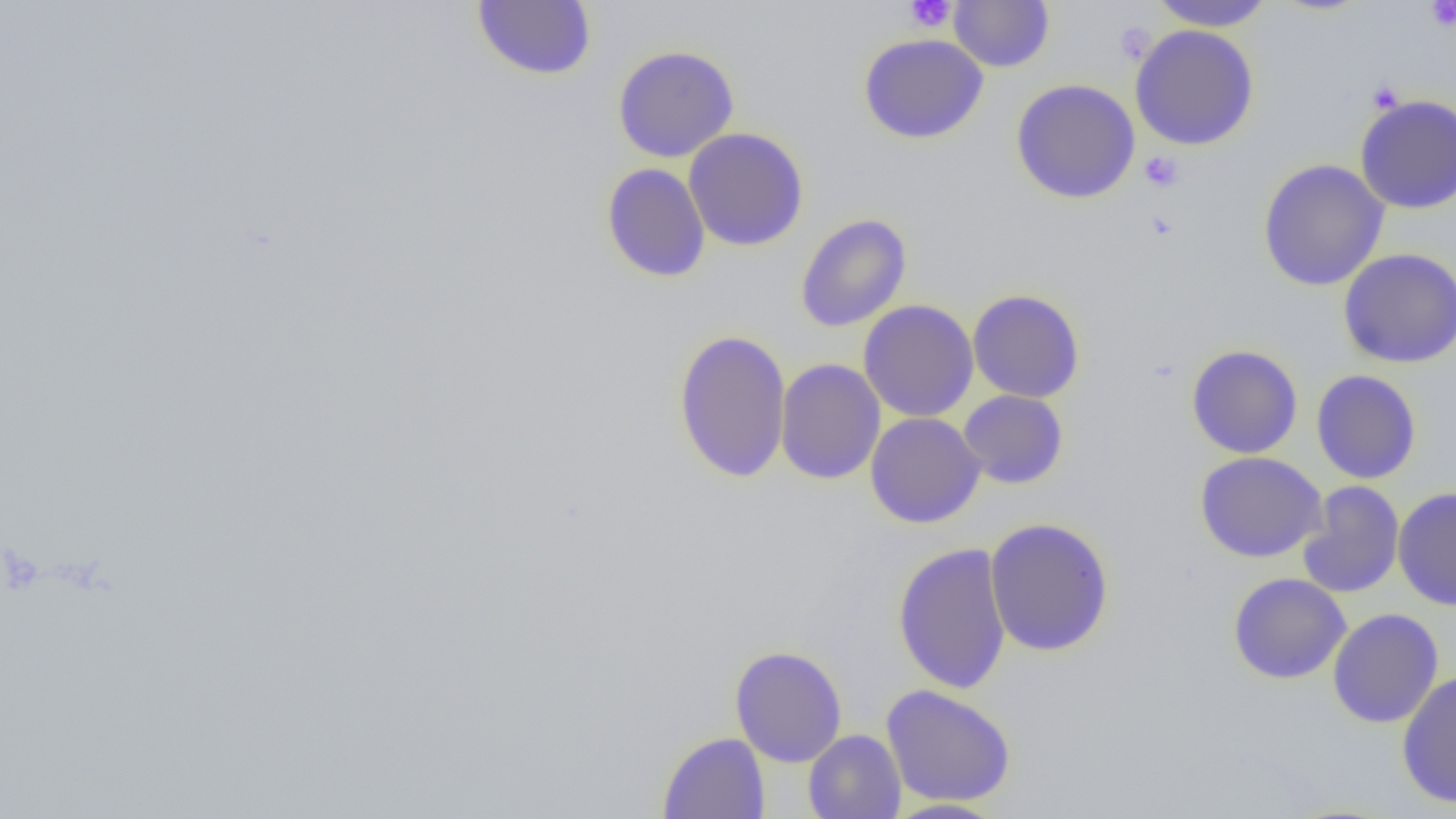
Summary:
  - Coordinate format: approximate bounding boxes as [x1, y1, x2, y2] in pixels
  - Platelet locations: [904, 0, 956, 32], [1425, 0, 1456, 31], [1116, 22, 1156, 65], [1139, 150, 1185, 193]
  - Uninfected red blood cell locations: [471, 0, 597, 82], [949, 0, 1054, 72], [1149, 0, 1274, 31], [1130, 24, 1259, 150], [858, 33, 989, 144], [612, 45, 739, 162], [1011, 78, 1141, 204], [1355, 94, 1456, 213], [683, 128, 809, 252], [1257, 158, 1390, 291], [601, 162, 711, 283], [795, 213, 912, 332], [1338, 248, 1456, 368], [968, 289, 1085, 403], [858, 299, 979, 422], [672, 328, 792, 483], [1186, 344, 1303, 459], [775, 358, 886, 485], [1311, 369, 1422, 484], [958, 390, 1068, 489], [865, 411, 986, 528], [1195, 451, 1326, 562], [1297, 481, 1405, 599], [1393, 487, 1456, 611], [985, 517, 1115, 657], [892, 542, 1012, 694], [1228, 572, 1351, 684], [1327, 608, 1444, 728], [730, 645, 847, 767], [1396, 670, 1456, 808], [880, 684, 1017, 807], [803, 729, 906, 818], [658, 731, 771, 819], [884, 798, 1007, 819]
  - Slide-level diagnosis: negative for blood parasites
  - Modality: light microscopy
  - Image size: 1456×819 pixels
  - Magnification: 1000x
  - Field of view: one of a larger specimen
  - Preparation: thin blood film